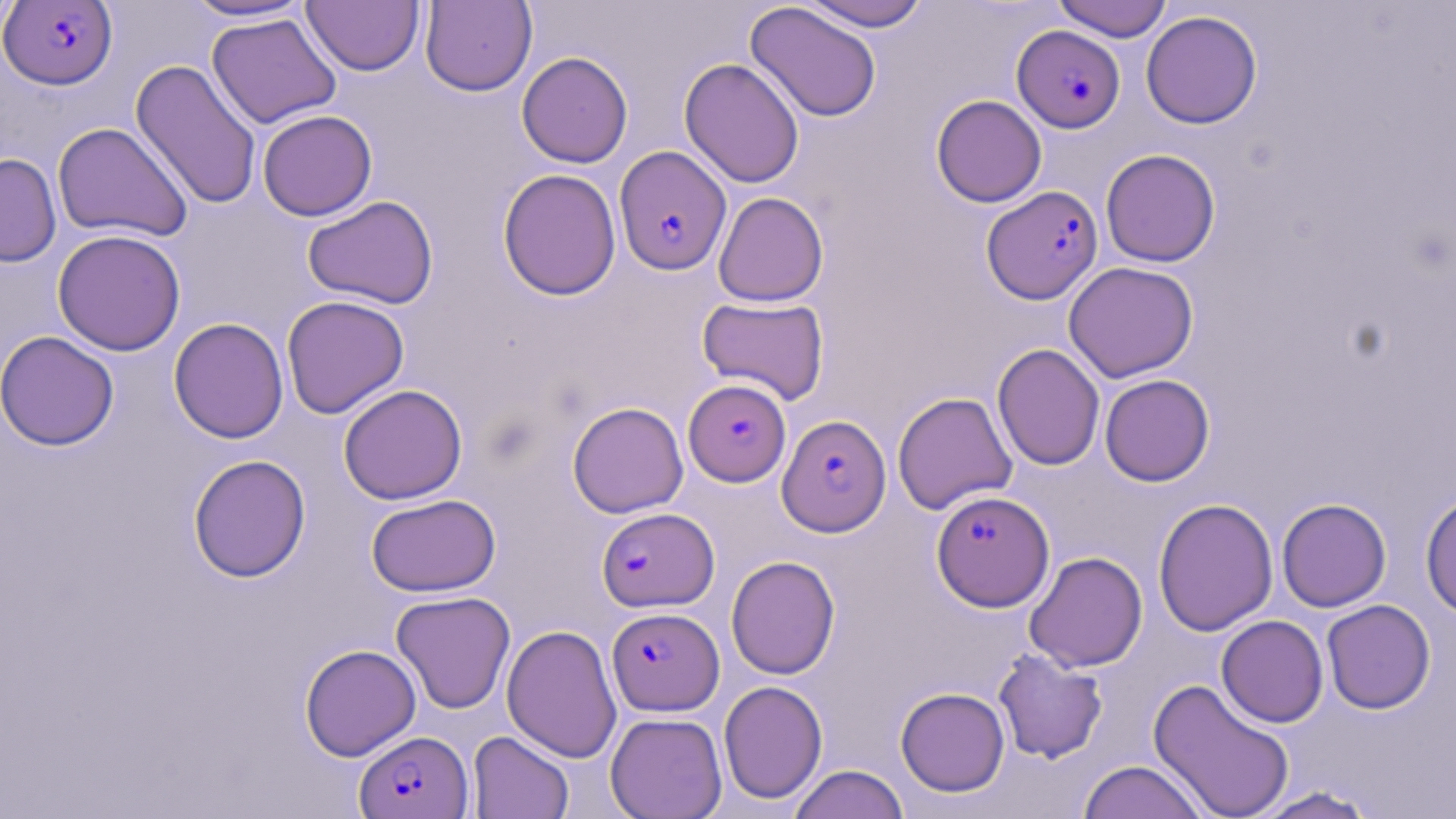

slide_level_diagnosis: Plasmodium falciparum
stain: May-Grünwald-Giemsa
image_size: 1456×819 pixels
modality: light microscopy
field_of_view: one of a larger specimen
preparation: thin blood smear
plasmodium_falciparum_infected_red_blood_cell_locations: 'approximate bounding boxes as (x1, y1, x2, y2) in pixels: (0, 1, 118, 89), (1012, 25, 1125, 132), (614, 146, 731, 275), (982, 185, 1103, 304), (684, 379, 791, 486), (777, 414, 890, 536), (932, 490, 1054, 611), (597, 507, 719, 611), (607, 607, 724, 715), (354, 730, 472, 819)'
uninfected_red_blood_cell_locations: 'approximate bounding boxes as (x1, y1, x2, y2) in pixels: (181, 0, 316, 23), (799, 0, 933, 31), (1052, 0, 1172, 42), (302, 1, 424, 75), (420, 1, 537, 96), (745, 2, 883, 123), (1141, 10, 1262, 129), (206, 12, 342, 129), (516, 51, 633, 168), (679, 57, 805, 188), (130, 58, 262, 211), (931, 94, 1047, 207), (257, 109, 377, 221), (52, 122, 193, 243), (1100, 149, 1221, 267), (0, 153, 61, 267), (497, 168, 622, 301), (713, 191, 829, 306), (302, 195, 439, 309), (51, 229, 186, 356), (1063, 262, 1199, 382), (281, 295, 409, 419), (697, 296, 830, 404), (169, 317, 289, 444), (0, 331, 119, 451), (992, 343, 1105, 471), (1100, 374, 1215, 486), (339, 384, 467, 505), (892, 392, 1017, 515), (567, 402, 688, 518), (187, 454, 311, 582), (1420, 491, 1456, 619), (366, 493, 501, 597), (1153, 497, 1278, 637), (1276, 498, 1392, 612), (1024, 551, 1147, 672), (726, 555, 840, 680), (390, 591, 516, 714), (1321, 599, 1436, 714), (1216, 615, 1328, 728), (501, 624, 622, 763), (299, 644, 421, 761), (992, 648, 1108, 764), (1148, 677, 1296, 819), (718, 680, 828, 805), (895, 687, 1010, 796), (605, 712, 727, 818), (467, 731, 574, 819), (1078, 760, 1208, 819), (787, 764, 909, 819), (1248, 786, 1379, 818)'
magnification: 1000x